Comment on the morphology of the red blood cells.
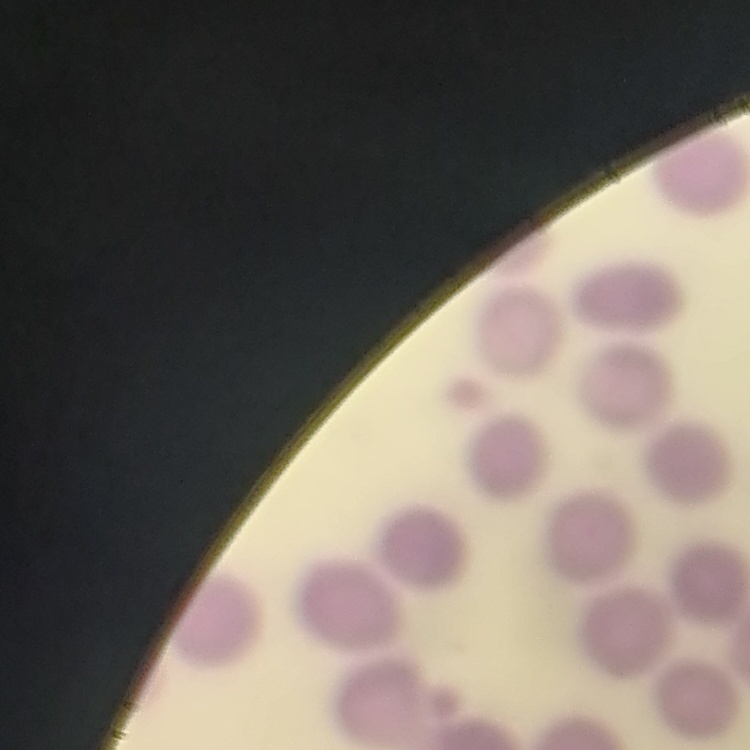
No rouleaux formation.

Square crop of a larger photomicrograph. Stained with either Field's or Giemsa. Thin blood smear.